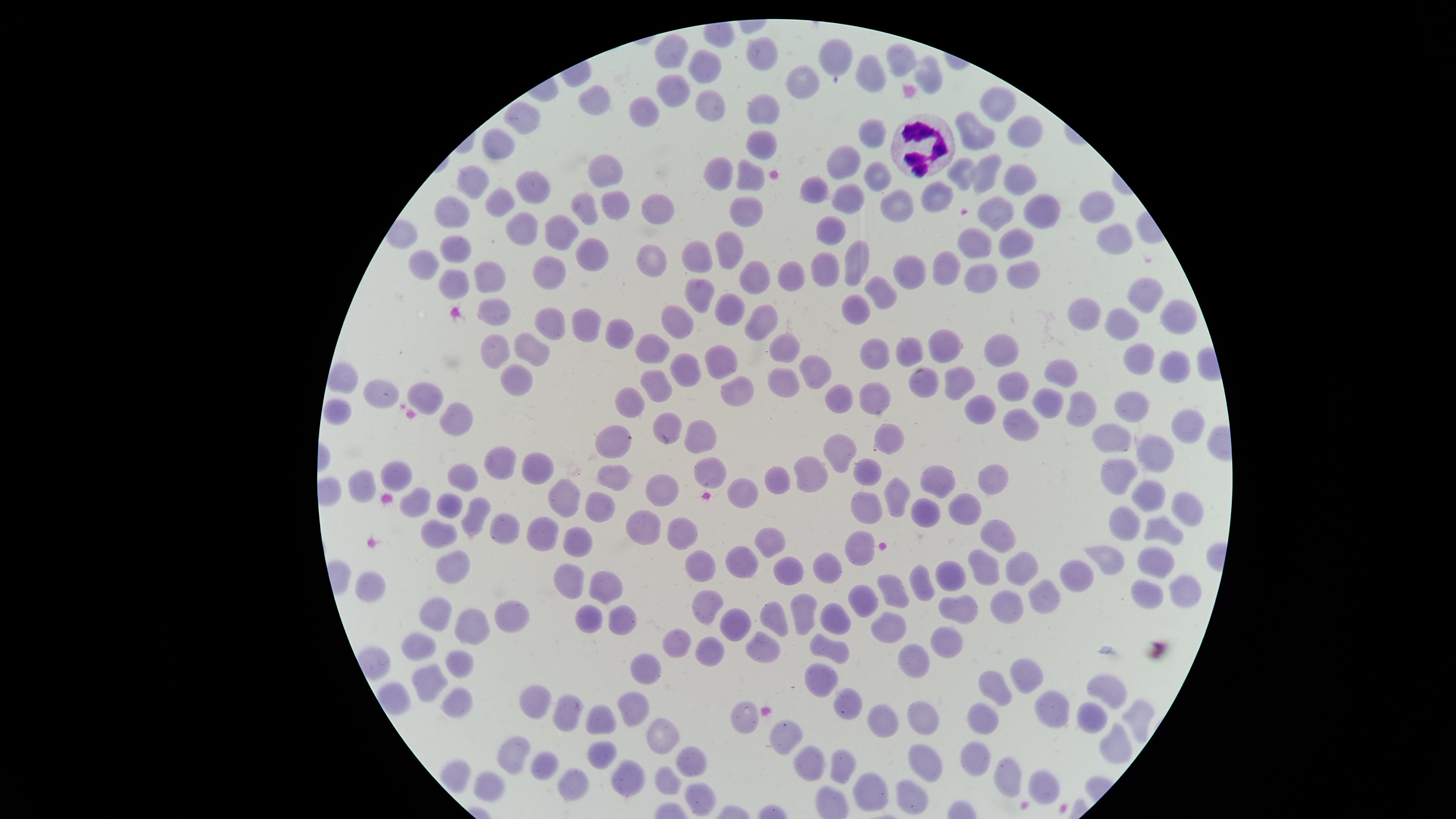

{
  "stain": "Giemsa",
  "uninfected_red_blood_cells": "approximate marker points as [x, y] in pixels: [759, 51], [673, 54], [837, 58], [902, 61], [702, 64], [871, 75], [929, 75], [798, 78], [673, 86], [600, 100], [706, 103], [995, 104], [647, 107], [765, 110], [525, 117], [1020, 131], [867, 133], [972, 133], [762, 143], [500, 146], [846, 161], [991, 169], [877, 170], [1019, 171], [965, 172], [605, 173], [754, 176], [723, 180], [476, 184], [534, 189], [816, 189], [940, 194], [849, 197], [894, 201], [503, 205], [657, 206], [1034, 206], [578, 207], [456, 208], [611, 208], [1093, 209], [997, 214], [746, 215], [519, 226], [832, 227], [565, 236], [1110, 239], [1013, 241], [978, 242], [457, 247], [732, 247], [595, 252], [698, 260], [857, 260], [655, 262], [425, 264], [1019, 269], [907, 270], [945, 270], [794, 272], [826, 272], [552, 273], [752, 274], [488, 276], [982, 282], [447, 285], [882, 290], [695, 293], [1144, 293], [732, 304], [858, 308], [496, 309], [1091, 316], [1174, 318], [551, 321], [677, 322], [765, 322], [1124, 323], [580, 332], [620, 333], [948, 345], [786, 346], [996, 346], [907, 348], [651, 349], [498, 350], [537, 351], [876, 356], [721, 362], [1140, 364], [1174, 365], [813, 370], [1061, 372], [687, 373], [514, 374], [961, 379], [342, 380], [781, 380], [926, 380], [656, 388], [1013, 388], [738, 391], [384, 396], [875, 396], [421, 397], [626, 397], [841, 397], [1050, 400], [1132, 402], [977, 405], [1079, 405], [339, 408], [457, 422], [667, 422], [1186, 422], [1025, 427], [704, 433], [889, 434], [1109, 436], [608, 438], [846, 449], [1158, 451], [494, 463], [540, 467], [1117, 467], [816, 470], [396, 471], [618, 472], [714, 472], [867, 473], [457, 475], [780, 476], [930, 480], [992, 482], [359, 486], [659, 487], [562, 493], [738, 493], [1141, 493], [893, 497], [421, 499], [866, 499], [449, 505], [927, 505], [969, 505], [600, 506], [1184, 509], [475, 516], [1129, 518], [503, 524], [646, 526], [541, 528], [684, 529], [1167, 530], [996, 532], [441, 533], [577, 539], [773, 544], [861, 544], [745, 556], [1112, 557], [1155, 559], [1022, 565], [453, 566], [699, 568], [827, 568], [985, 569], [794, 571], [569, 577], [954, 577], [1082, 579], [920, 581], [373, 583], [605, 583], [893, 593], [1052, 595], [1144, 595], [1178, 595], [868, 599], [1007, 605], [962, 606], [704, 607], [796, 610], [440, 613], [511, 613], [624, 616], [776, 617], [583, 619], [833, 619], [738, 623], [473, 629], [893, 632], [953, 636], [677, 643], [421, 644], [715, 648], [761, 648], [831, 648], [917, 660], [458, 661], [822, 672], [644, 673], [1029, 676], [429, 677], [1109, 689], [995, 692], [391, 696], [849, 698], [452, 702], [535, 707], [632, 708], [1046, 712], [565, 713], [1089, 716], [740, 718], [923, 719], [986, 720], [1135, 720], [599, 722], [885, 726], [662, 731], [784, 737], [1115, 746], [508, 759], [598, 760], [692, 760], [979, 760], [546, 763], [923, 764], [805, 765], [841, 766], [1008, 776], [666, 780], [629, 782], [491, 785], [1046, 785], [567, 787], [871, 795], [696, 796], [913, 802]",
  "image_size": "1456×819 pixels",
  "presence": "no malaria parasites detected",
  "field_of_view": "single",
  "visible_region": "circular",
  "white_blood_cells": "approximate marker points as [x, y] in pixels: [927, 148]",
  "capture": "smartphone photograph through the microscope eyepiece",
  "preparation": "thin blood smear"
}